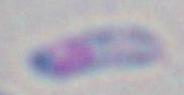

modality = micrograph
identification = Toxoplasma gondii
magnification = 1000x